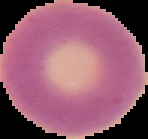
image_type: segmented cell region on a black background
image_size: 148×139 pixels
preparation: thin blood film
malaria_status: uninfected